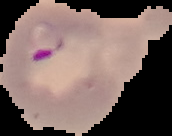
image type = segmented cell region on a black background
image size = 172×136 pixels
preparation = thin blood smear
malaria status = parasitized